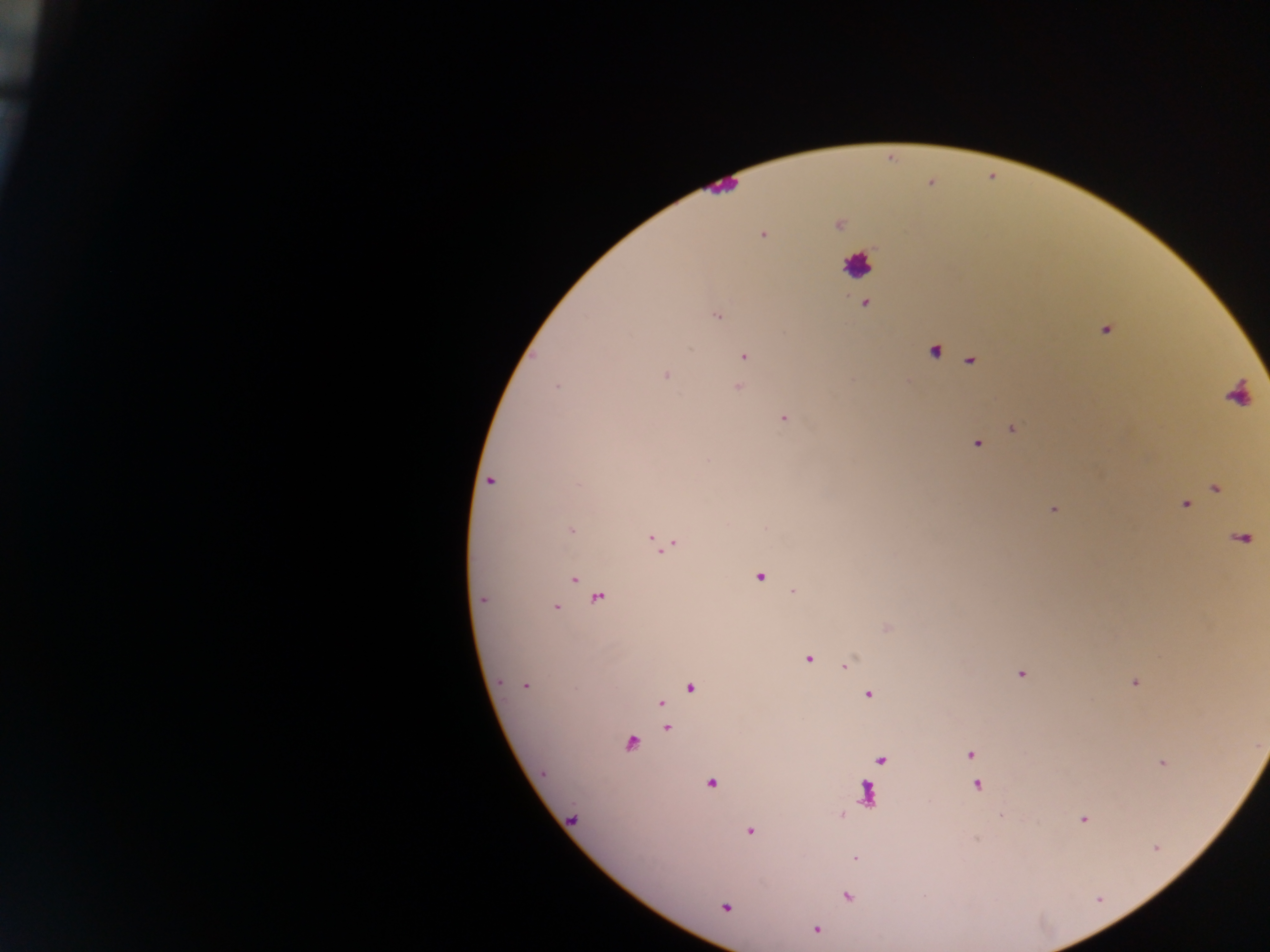
Approximate centers as x y in pixels. Leukocyte locations: 859 265. Malaria parasite locations: 762 235; 866 305; 717 317; 1106 331; 690 348; 744 356; 666 375; 557 387; 737 388; 784 418; 1013 429; 977 443; 490 481; 1216 489; 1185 505; 1054 509; 571 531; 663 543; 760 576; 574 579; 793 592; 597 599; 483 600; 556 607; 807 659; 846 666; 1021 674; 1135 683; 526 685; 689 688; 868 694; 660 703; 665 728; 630 743; 970 754; 882 761; 1162 763; 712 784; 977 786; 867 789; 1083 819; 749 832; 1156 848; 856 858; 847 896; 726 907; 816 929. Collected in Ghana. Image is 1270×952 pixels. Thick blood smear. Mobile-phone photograph taken through the microscope. One field of view.